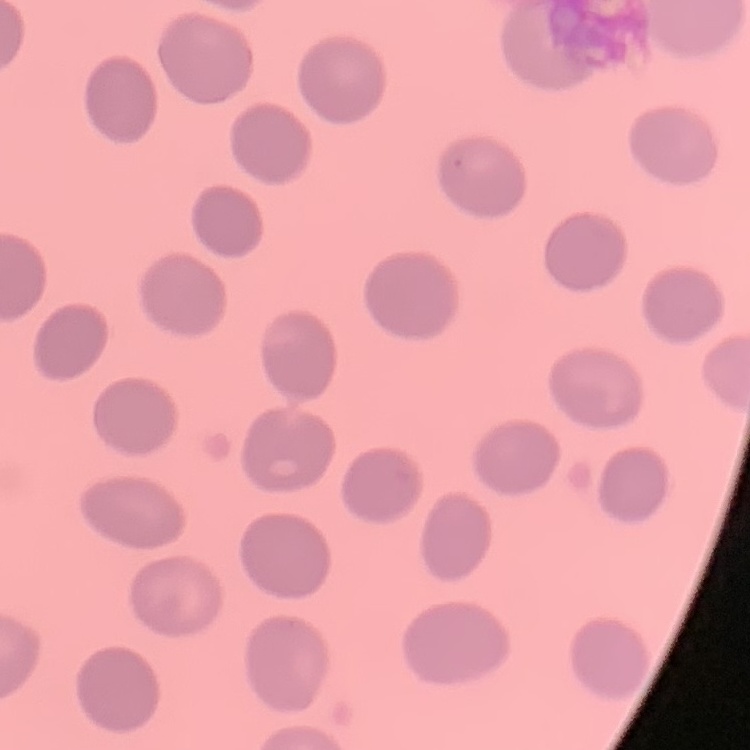

The erythrocytes show no rouleaux formation. Thin blood smear. One tile cut from a larger photomicrograph. Field's or Giemsa stain.